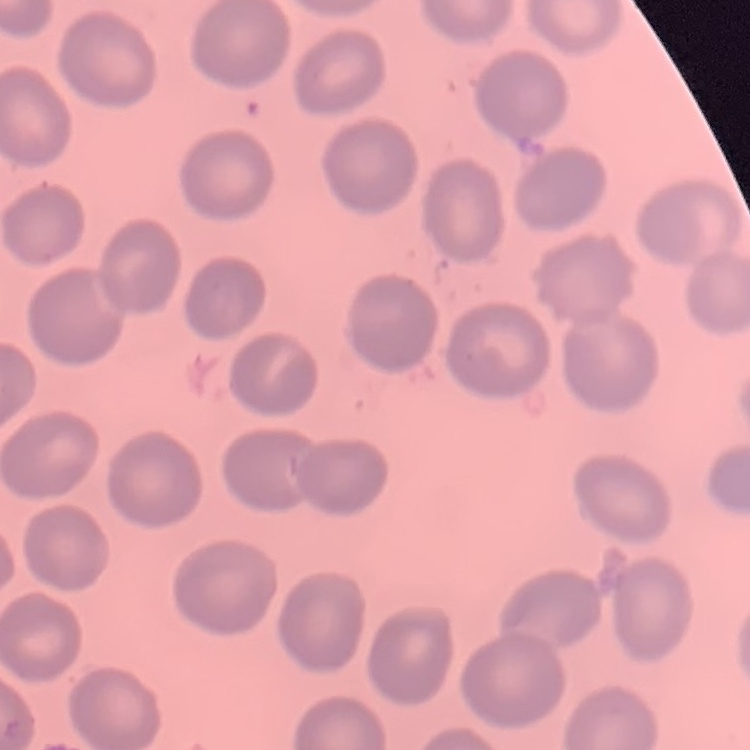

Summary:
  - Erythrocyte morphology: no rouleaux formation
  - Preparation: thin blood film
  - Stain: Field's or Giemsa
  - Image type: one tile cut from a larger photomicrograph